Comment on the morphology of the erythrocytes.
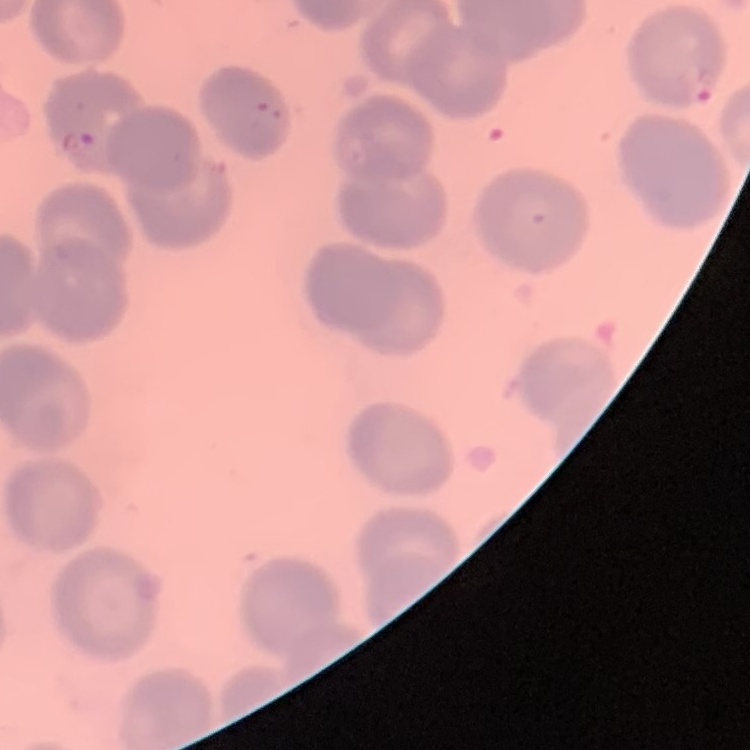
They show no rouleaux formation.

Thin blood smear. Field's or Giemsa stain. One tile cut from a larger photomicrograph.